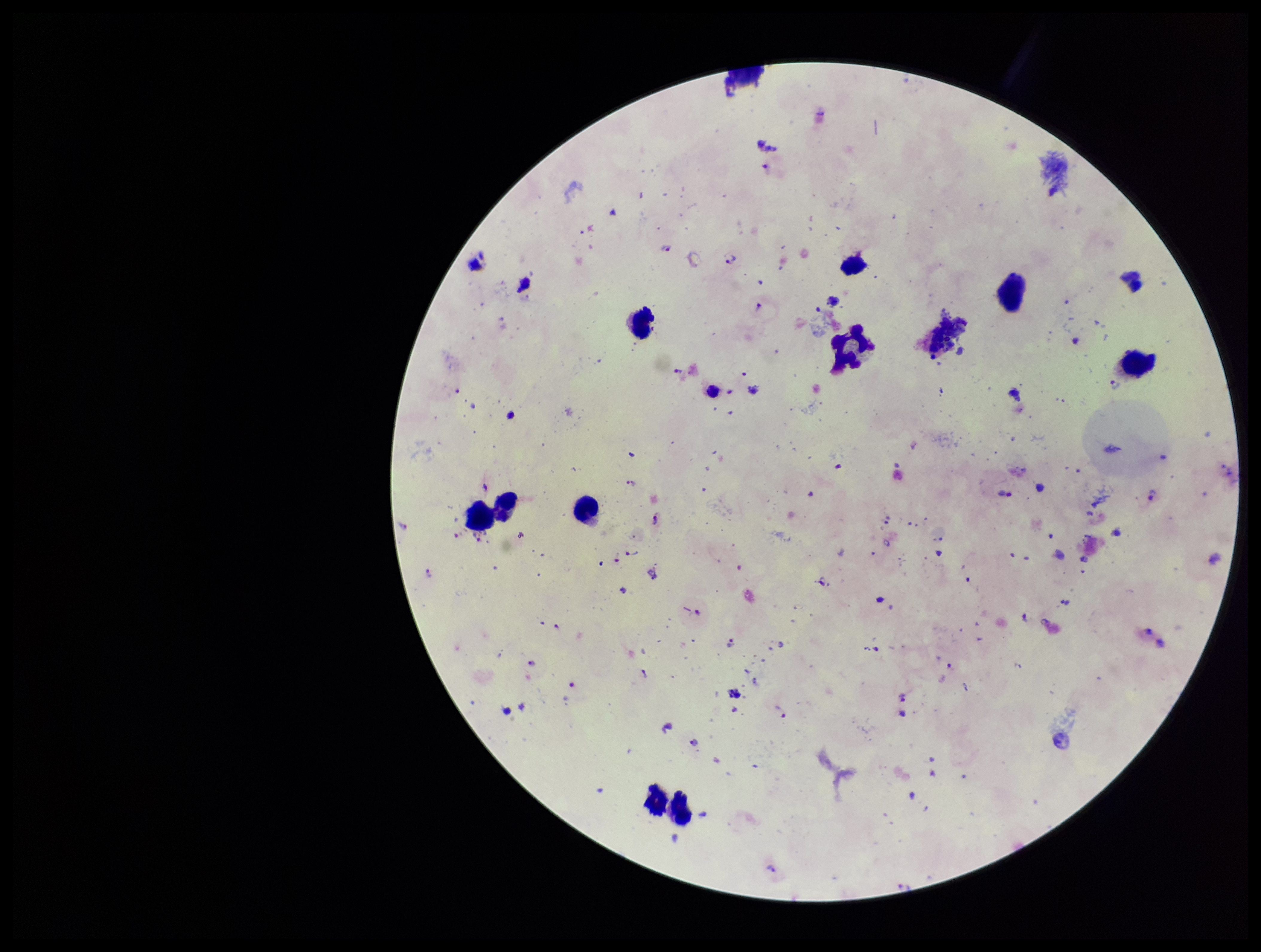

Plasmodium parasites: detected. Preparation: thick. Parasite count: 21. Species reported for this patient: Plasmodium falciparum. Patient malaria status: positive. Image is 1261×952 pixels. Leukocyte count: 10. Giemsa stain. Smartphone photograph taken through the eyepiece of a microscope. Single field of view.